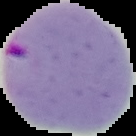

Image is 136×136 pixels. Malaria status: parasitized. The area outside the segmented cell region is set to black. From a thin blood film.